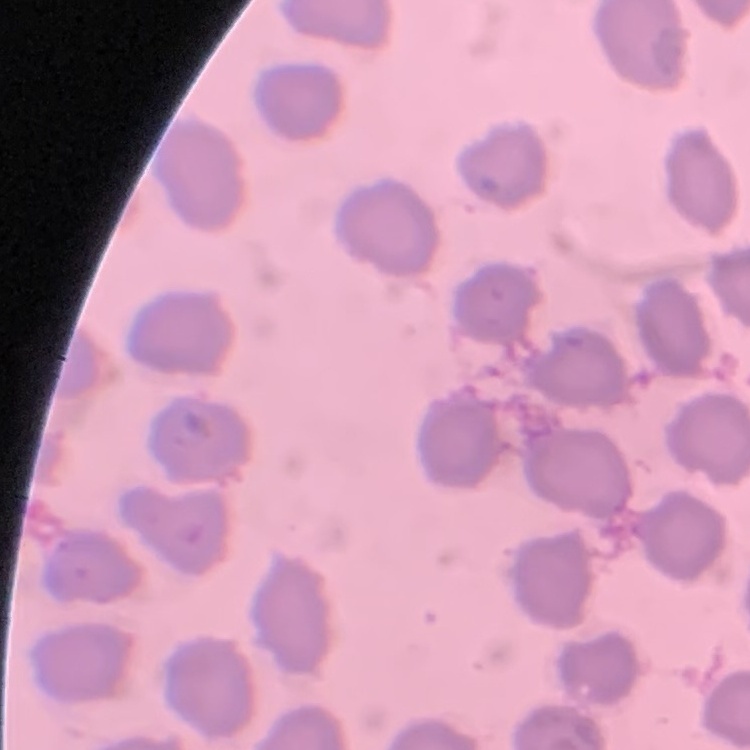

The red blood cells exhibit no rouleaux formation. One tile cut from a larger photomicrograph. Field's or Giemsa stain. Thin blood film.